Outline platelets.
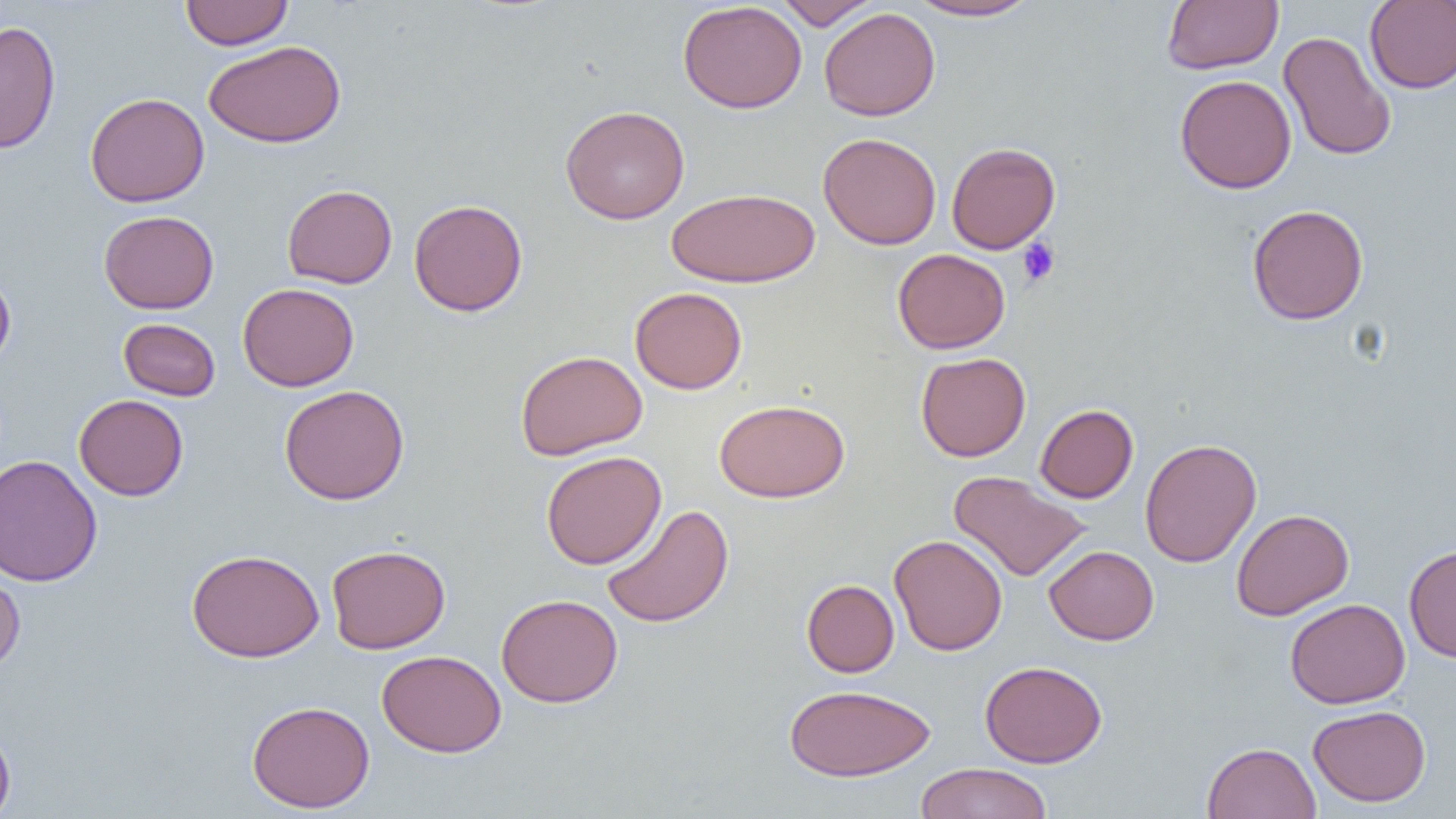

Approximate bounding boxes as (x1,y1)-(x2,y2) corner pairs in pixels.
Platelets: (1017,238)-(1060,287).

Uninfected red blood cell locations: (180,0)-(293,50), (774,0)-(881,30), (905,0)-(1041,22), (1162,0)-(1283,74), (677,1)-(808,114), (1364,1)-(1456,93), (818,7)-(940,121), (1,19)-(60,155), (1279,30)-(1396,162), (204,40)-(346,148), (1174,75)-(1297,194), (85,92)-(209,208), (559,104)-(690,224), (817,132)-(942,249), (946,141)-(1061,254), (282,184)-(398,288), (666,187)-(821,288), (408,199)-(528,316), (1247,204)-(1369,325), (98,210)-(219,314), (893,248)-(1010,354), (0,268)-(16,371), (238,283)-(359,391), (630,287)-(747,394), (118,318)-(220,400), (515,350)-(647,460), (916,352)-(1031,461), (279,384)-(409,505), (74,394)-(188,501), (714,398)-(849,502), (1035,404)-(1138,503), (1140,438)-(1262,567), (540,450)-(667,569), (0,454)-(103,588), (949,470)-(1091,582), (601,504)-(735,628), (1231,508)-(1354,621), (889,534)-(1008,656), (325,544)-(450,654), (1404,544)-(1456,663), (1044,545)-(1159,645), (186,548)-(324,662), (0,568)-(25,677), (801,579)-(900,677), (496,594)-(623,708), (1285,598)-(1410,708), (376,650)-(506,757), (980,660)-(1108,768), (783,684)-(935,782), (246,700)-(375,813), (1308,704)-(1431,807), (0,724)-(16,819), (1202,741)-(1321,819), (914,763)-(1054,819). Slide-level diagnosis: no evidence of blood parasites. Image is 1456×819 pixels. Single field of view. Optical microscopy. 1000x magnification. Thin blood film.